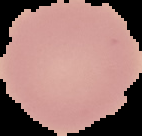
malaria status = uninfected
image type = segmented cell region with the area outside set to black
preparation = thin blood smear
image size = 142×136 pixels